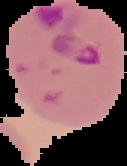

Summary:
  - Image type: segmented cell region with the area outside set to black
  - Preparation: thin blood smear
  - Malaria status: parasitized
  - Image size: 127×166 pixels